State which cell type is depicted.
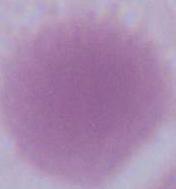
This is an erythrocyte.

{
  "magnification": "1000x",
  "modality": "micrograph"
}